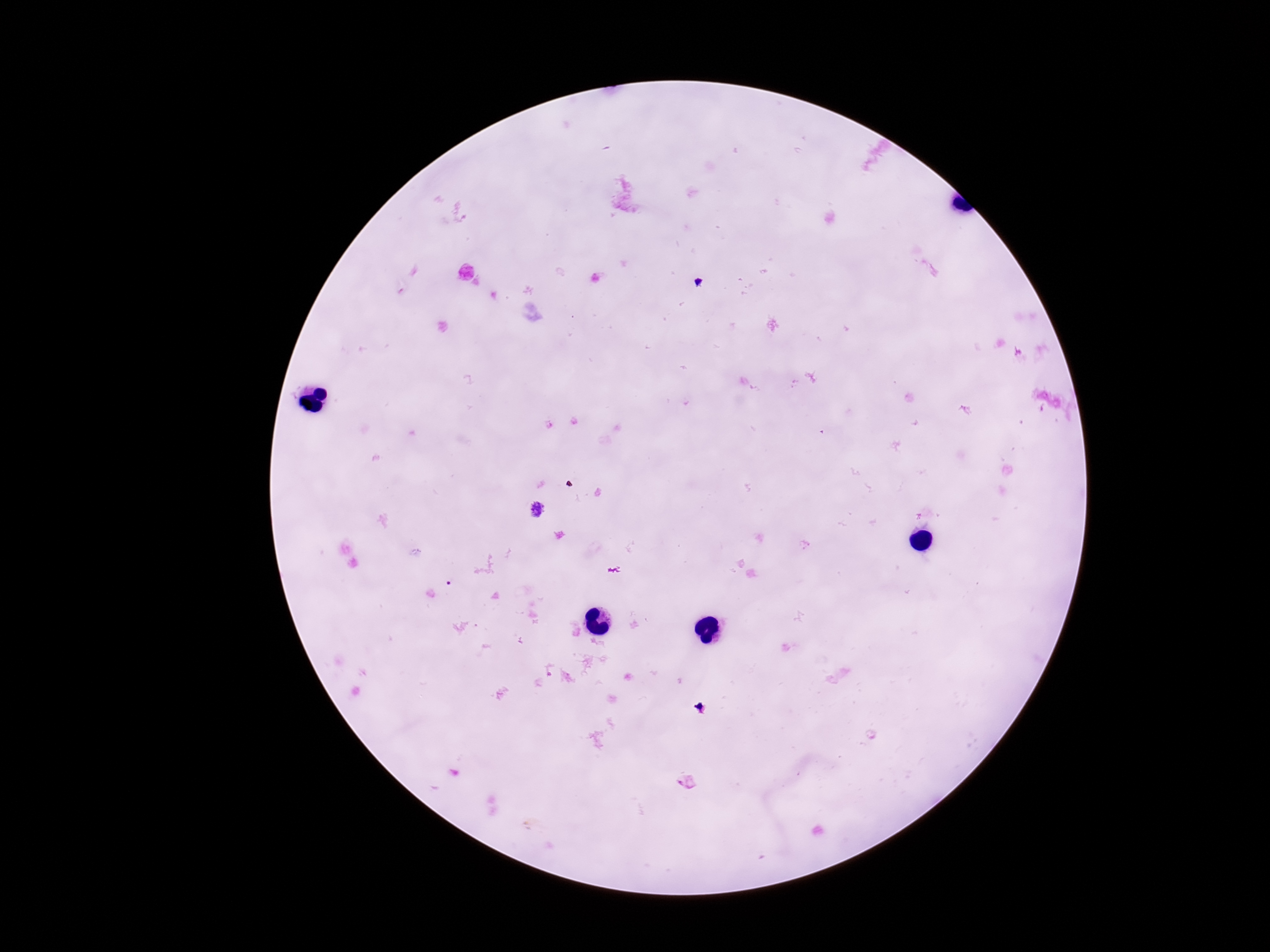

Approximate centers as {x, y} in pixels. Plasmodium parasite locations: {537, 510}. Image is 1270×952 pixels. Patient malaria status: infected. 100x magnification. One field from this slide. Photographed through the microscope eyepiece with a smartphone camera. Giemsa stain. Thick blood smear.